Assess this cell for malaria.
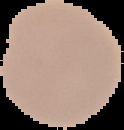

It is parasitized.

image size = 124×130 pixels
preparation = thin blood film
image type = segmented cell region with the area outside set to black